Name the parasite shown.
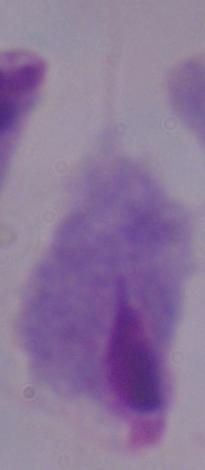

A trichomonad.

Photomicrograph. Captured at 1000x magnification.